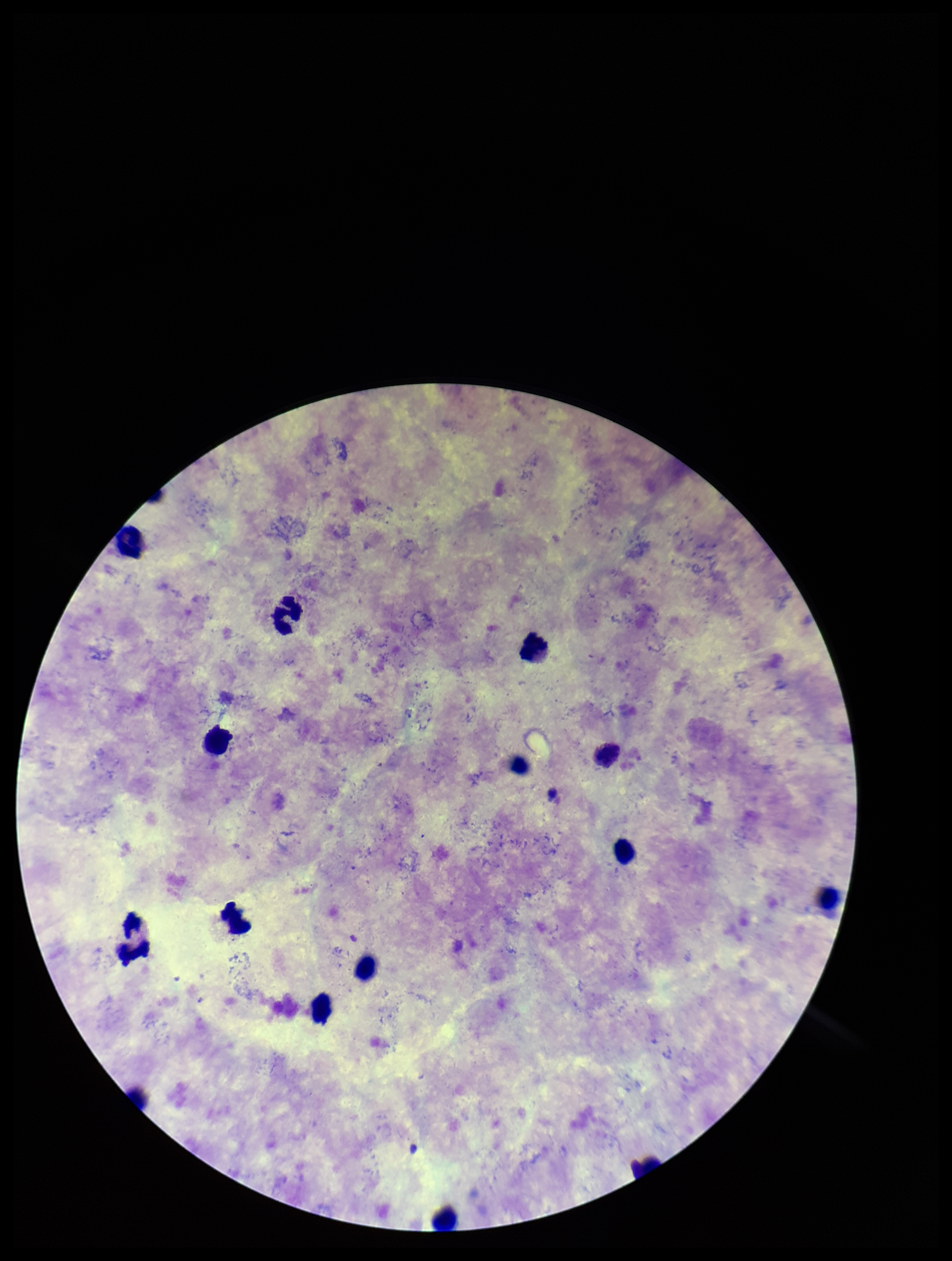
{
  "patient_malaria_status": "infected",
  "capture": "smartphone photograph through the microscope eyepiece",
  "preparation": "thick",
  "species_reported_for_this_patient": "Plasmodium vivax",
  "leukocyte_count": 13,
  "stain": "Giemsa",
  "image_size": "952×1261 pixels",
  "parasite_count": 0,
  "plasmodium_parasites": "none identified",
  "field_of_view": "one from this slide"
}